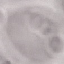

malaria_status: uninfected
image_type: automatically extracted cell patch, resized to 64 × 64 pixels
stain: Giemsa
capture: smartphone camera at the microscope eyepiece
preparation: thin smear